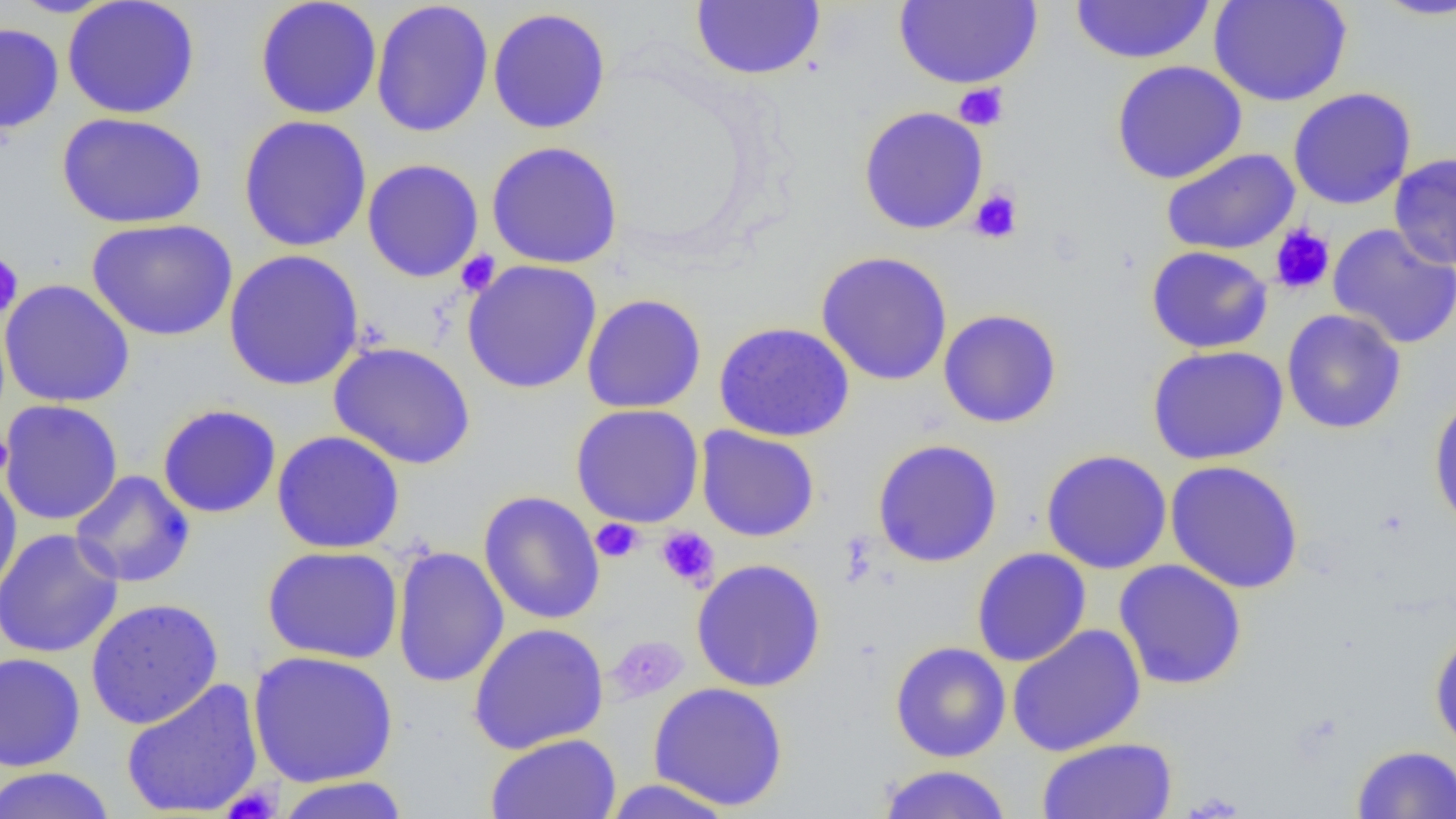
Summary:
  - Coordinate format: approximate bounding boxes as (x1,y1)-(x2,y2) corner pairs in pixels
  - Uninfected red blood cell locations: (62,0)-(200,119), (254,0)-(383,119), (1208,0)-(1353,106), (1368,0)-(1456,21), (370,1)-(494,138), (691,1)-(826,81), (894,1)-(1042,88), (1069,1)-(1217,65), (487,7)-(612,134), (0,21)-(64,134), (1111,59)-(1248,184), (1287,87)-(1416,210), (857,106)-(989,235), (56,112)-(207,228), (237,114)-(373,253), (485,141)-(623,269), (1161,147)-(1300,256), (1388,151)-(1456,270), (362,158)-(484,283), (86,217)-(238,341), (1327,223)-(1456,349), (1145,245)-(1273,353), (223,248)-(364,392), (815,250)-(953,386), (462,259)-(602,394), (0,279)-(135,408), (581,293)-(707,414), (938,308)-(1062,428), (1281,308)-(1407,435), (714,321)-(855,442), (328,342)-(477,469), (1147,344)-(1289,465), (1428,393)-(1456,534), (0,399)-(124,526), (157,403)-(282,519), (571,403)-(704,528), (695,426)-(820,542), (271,430)-(405,554), (872,438)-(1003,567), (1040,449)-(1173,574), (1165,460)-(1304,594), (70,470)-(196,588), (0,471)-(23,603), (478,490)-(606,625), (0,528)-(124,658), (262,545)-(403,664), (391,545)-(509,688), (971,548)-(1092,667), (691,558)-(827,693), (1113,559)-(1248,690), (85,598)-(224,729), (468,622)-(609,754), (1007,624)-(1146,757), (1429,627)-(1456,754), (889,641)-(1011,762), (247,650)-(399,787), (0,652)-(86,772), (121,677)-(264,818), (648,682)-(789,811), (485,732)-(621,819), (1036,737)-(1178,819), (1351,745)-(1455,819), (877,764)-(1013,819), (0,766)-(117,819), (274,776)-(410,819), (601,779)-(737,818)
  - Platelet locations: (953,83)-(1009,130), (968,188)-(1023,244), (1269,223)-(1335,296), (455,250)-(501,296), (0,254)-(23,319), (0,432)-(14,479), (591,519)-(644,563), (655,526)-(720,589), (607,636)-(688,702), (222,784)-(281,819)
  - Slide-level diagnosis: no evidence of blood parasites
  - Field of view: single
  - Magnification: 1000x
  - Modality: light microscopy
  - Preparation: thin blood smear
  - Image size: 1456×819 pixels